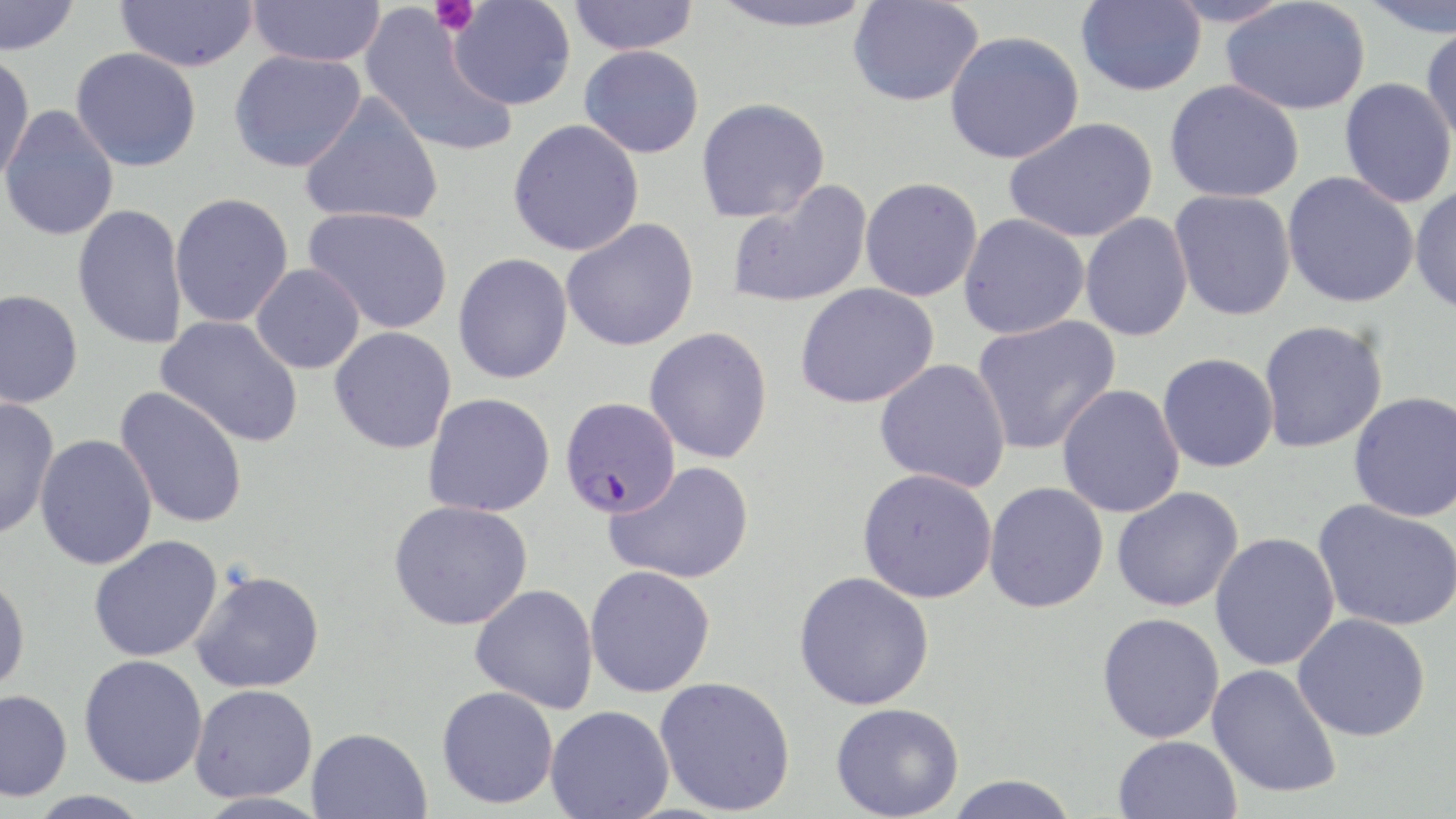
Summary:
  - Coordinate format: approximate bounding boxes as [x1, y1, x2, y2] in pixels
  - Uninfected red blood cell locations: [0, 0, 81, 56], [115, 0, 258, 72], [247, 0, 386, 68], [568, 0, 699, 55], [705, 0, 881, 33], [848, 0, 984, 107], [1076, 0, 1206, 97], [1164, 0, 1297, 28], [1357, 0, 1456, 38], [447, 1, 576, 111], [1220, 2, 1370, 115], [360, 7, 517, 158], [1421, 23, 1456, 149], [945, 31, 1084, 164], [579, 45, 705, 158], [70, 47, 202, 171], [229, 47, 366, 173], [0, 51, 35, 185], [1339, 78, 1456, 208], [1164, 79, 1304, 203], [299, 92, 444, 228], [696, 97, 830, 223], [1, 104, 120, 242], [1004, 117, 1159, 243], [507, 119, 645, 256], [1282, 172, 1420, 308], [860, 177, 983, 301], [727, 181, 872, 309], [1410, 186, 1456, 317], [1169, 189, 1296, 321], [169, 192, 294, 328], [72, 203, 189, 349], [303, 206, 454, 334], [958, 213, 1090, 339], [1079, 213, 1193, 342], [561, 218, 699, 351], [453, 253, 573, 384], [251, 263, 365, 374], [795, 283, 939, 409], [0, 289, 84, 409], [156, 315, 304, 447], [971, 315, 1121, 456], [1258, 320, 1388, 453], [329, 326, 457, 454], [644, 327, 773, 464], [1157, 352, 1279, 472], [874, 357, 1012, 492], [1057, 385, 1185, 519], [114, 386, 249, 530], [1348, 391, 1456, 522], [423, 393, 555, 517], [0, 397, 59, 539], [35, 434, 158, 570], [605, 461, 755, 585], [857, 468, 998, 603], [983, 481, 1109, 613], [1111, 486, 1245, 613], [1313, 499, 1456, 632], [389, 500, 533, 631], [1209, 532, 1340, 671], [89, 535, 223, 662], [585, 565, 715, 698], [190, 569, 325, 694], [793, 571, 935, 711], [0, 573, 30, 698], [470, 583, 599, 713], [1097, 612, 1225, 743], [1292, 612, 1431, 741], [79, 654, 208, 788], [1207, 663, 1342, 798], [654, 676, 796, 816], [189, 684, 318, 803], [437, 686, 559, 809], [0, 689, 73, 802], [831, 702, 965, 819], [545, 706, 674, 819], [307, 727, 432, 819], [1113, 735, 1242, 819], [944, 774, 1080, 819], [26, 790, 154, 818]
  - Platelet locations: [429, 0, 479, 36]
  - Plasmodium falciparum-infected red blood cell locations: [559, 396, 681, 520]
  - Slide-level diagnosis: Plasmodium falciparum
  - Field of view: single
  - Image size: 1456×819 pixels
  - Modality: light microscopy
  - Stain: May-Grünwald-Giemsa
  - Magnification: 1000x
  - Preparation: thin blood film